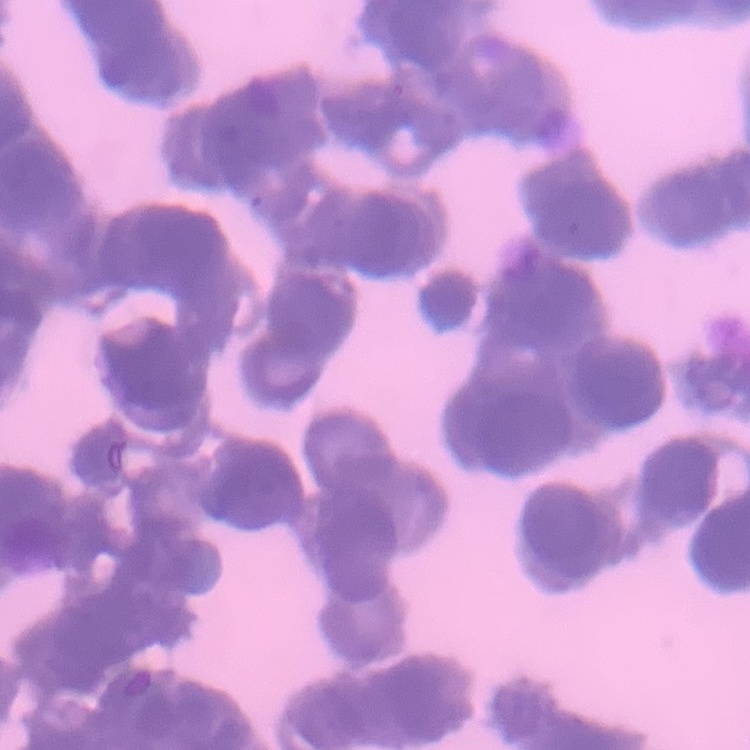

Summary:
  - Erythrocyte morphology: rouleaux formation
  - Image type: one tile cut from a larger photomicrograph
  - Preparation: thin blood film
  - Stain: Field's or Giemsa